Comment on the morphology of the red blood cells.
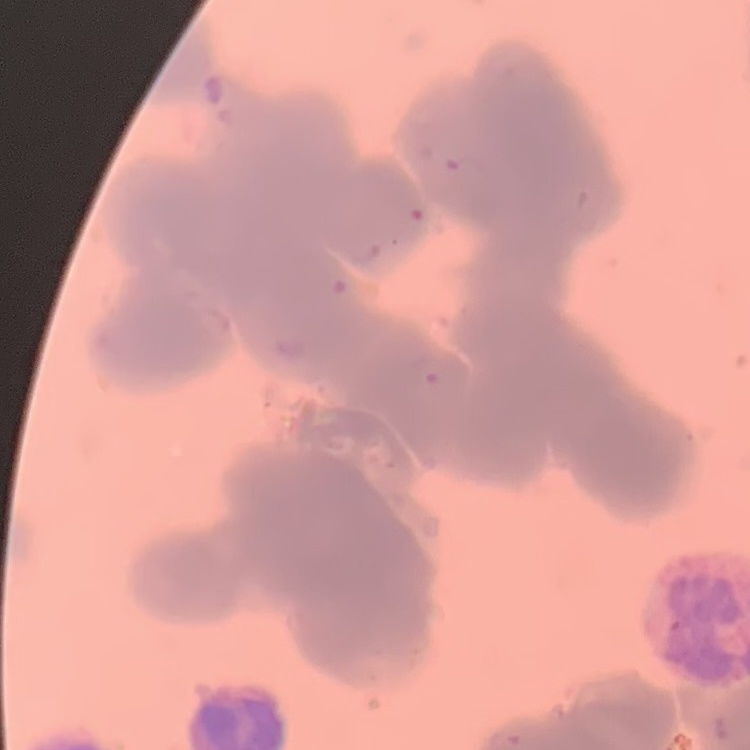

Rouleaux formation.

stain = Field's or Giemsa
image type = one tile cut from a larger photomicrograph
preparation = thin blood film